Name the parasite shown.
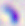

This is Toxoplasma gondii.

magnification = 400x
modality = micrograph